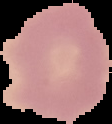

From a thin blood film. Cell region segmented out of the field of view; the surrounding area is masked to black. Result: negative for Plasmodium parasites. Image is 112×124 pixels.